Identify the cell.
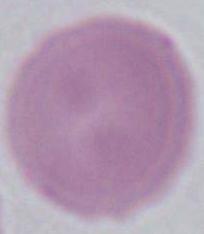

An erythrocyte.

Photomicrograph. Captured at 1000x magnification.